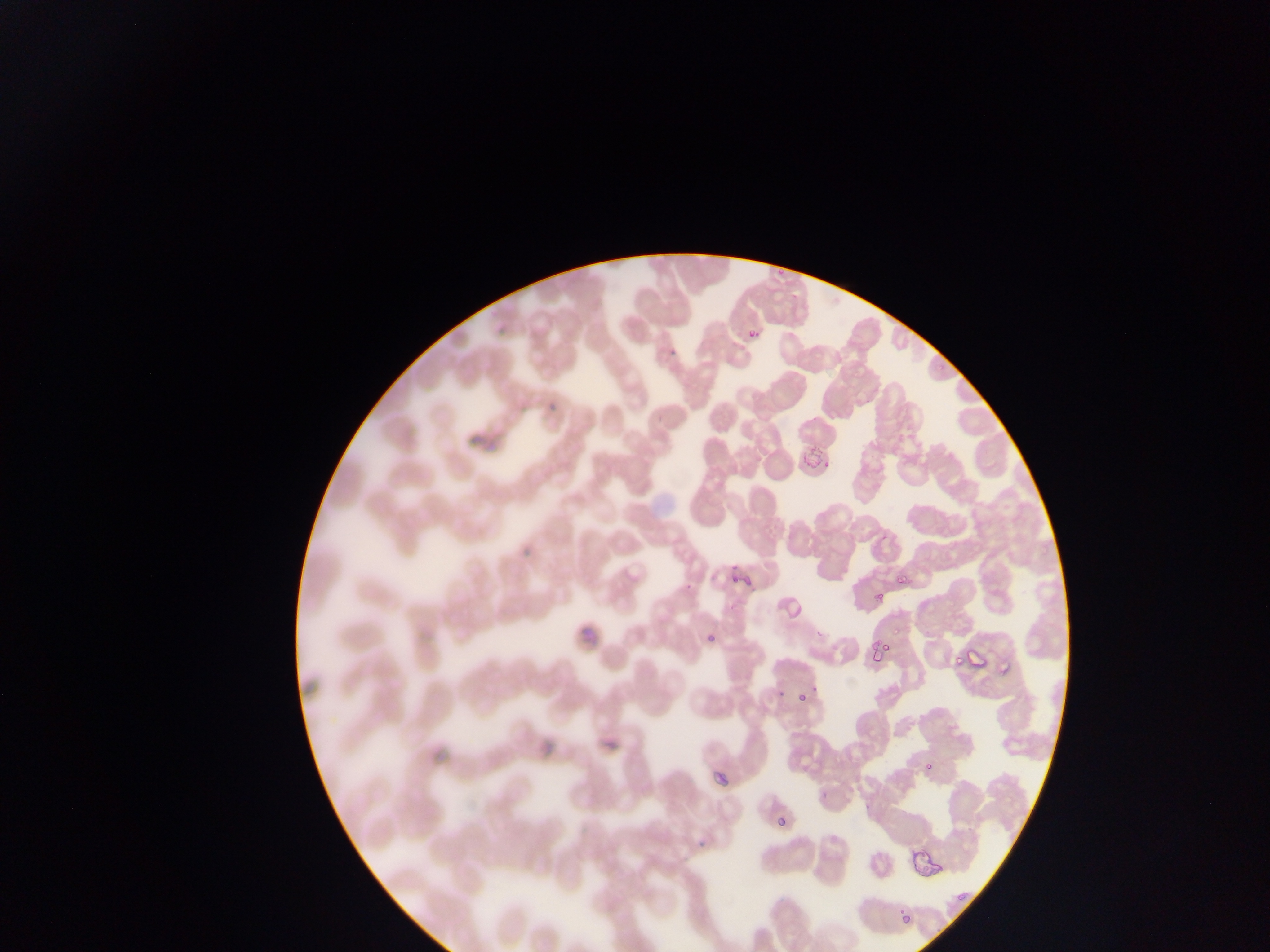
{
  "capture": "mobile-phone photograph through a microscope",
  "plasmodium_parasite_locations": "approximate bounding boxes as (left, top, right, bottom) in pixels: (776, 260, 789, 277), (741, 323, 765, 347), (494, 328, 507, 336), (669, 348, 678, 357), (935, 361, 948, 373), (517, 393, 528, 412), (548, 405, 559, 413), (795, 437, 828, 475), (878, 532, 889, 541), (520, 543, 530, 558), (727, 562, 738, 569), (730, 572, 742, 588), (893, 573, 910, 585), (742, 575, 751, 587), (683, 579, 697, 591), (874, 585, 892, 600), (778, 589, 817, 623), (730, 599, 740, 609), (896, 625, 906, 637), (703, 626, 718, 643), (813, 629, 824, 637), (870, 634, 895, 658), (962, 638, 995, 670), (949, 651, 966, 669), (996, 654, 1016, 678), (776, 683, 787, 697), (797, 694, 809, 707), (709, 759, 740, 788), (923, 760, 941, 773), (824, 779, 838, 796), (777, 817, 787, 830), (698, 819, 711, 846), (906, 829, 946, 882), (953, 886, 970, 909), (900, 911, 910, 923) | approximate (x, y) pixel centers of objects too small to bound: (816, 690)",
  "image_size": "1270×952 pixels",
  "field_of_view": "single",
  "preparation": "thin blood film",
  "country": "Ghana"
}